Point out leukocytes.
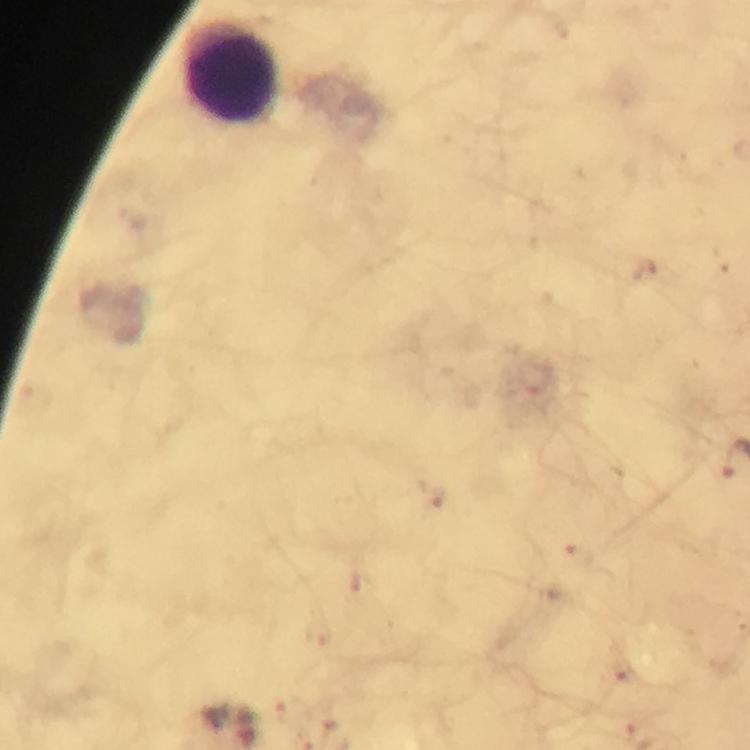
Approximate centers as (x, y) in pixels.
Leukocytes: (232, 73).

Plasmodium parasite locations: (431, 494). Immersion oil applied. From a diagnostic examination for malaria. Thick smear. Photographed with a smartphone mounted on the microscope. Image is 750×750 pixels. Cropped region of a single field of view. 100x magnification. Giemsa-stained preparation.